Comment on the morphology of the red blood cells.
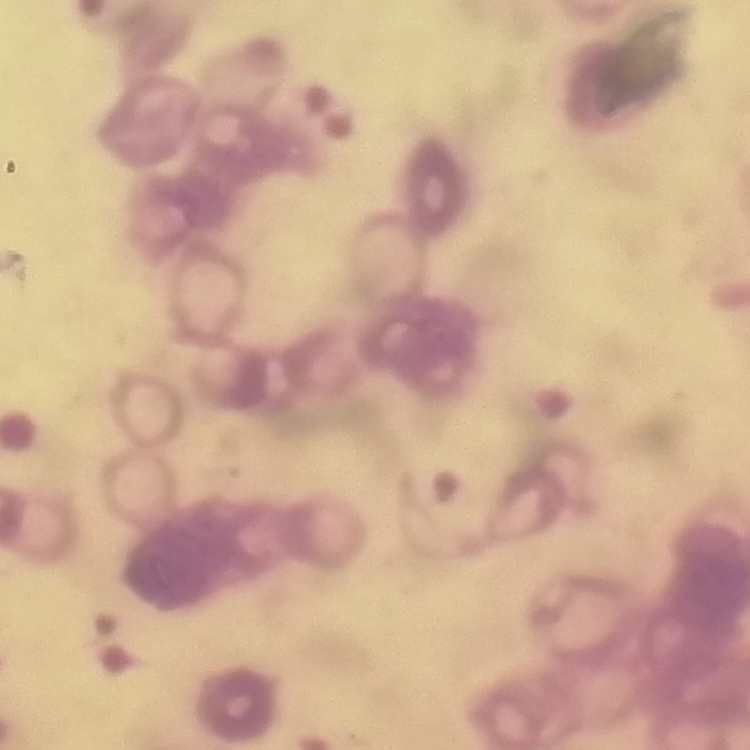

Rouleaux formation.

Summary:
  - Stain: Field's or Giemsa
  - Preparation: thin peripheral smear
  - Image type: one tile cut from a larger photomicrograph